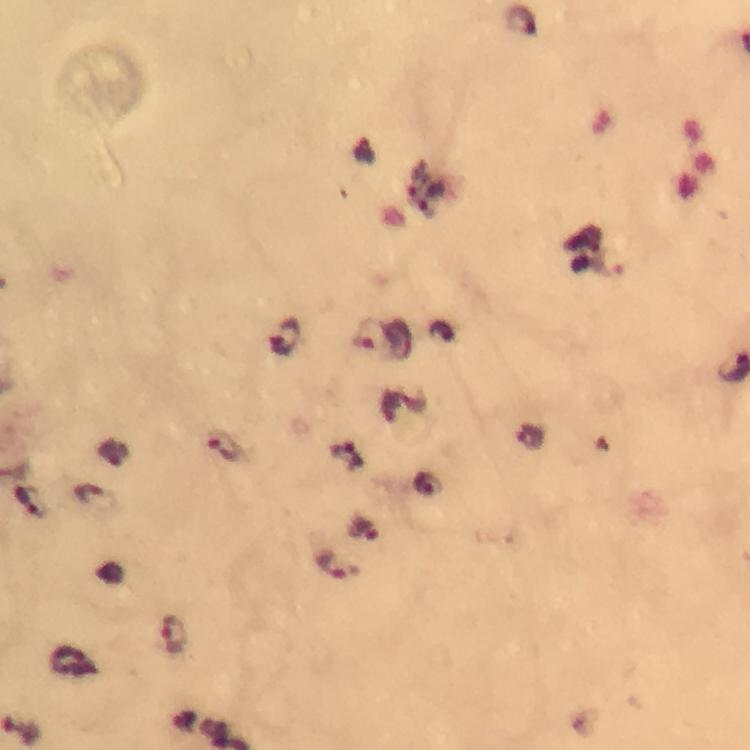
{
  "stain": "Giemsa",
  "capture": "smartphone camera through the microscope",
  "context": "from a malaria diagnostic workup",
  "magnification": "100x",
  "cropped_from": "one field of view",
  "image_size": "750×750 pixels",
  "immersion_oil": "applied",
  "plasmodium_parasite_locations": "approximate object centers, in pixels from the top-left corner: (x=522, y=22), (x=418, y=178), (x=608, y=262), (x=370, y=336), (x=283, y=338), (x=529, y=438), (x=226, y=448), (x=346, y=456), (x=427, y=483), (x=89, y=494), (x=28, y=498), (x=329, y=565), (x=175, y=636)",
  "preparation": "thick blood film"
}